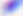
Summary:
  - Magnification: 400x
  - Modality: photomicrograph
  - Identification: Toxoplasma gondii